Identify the parasite.
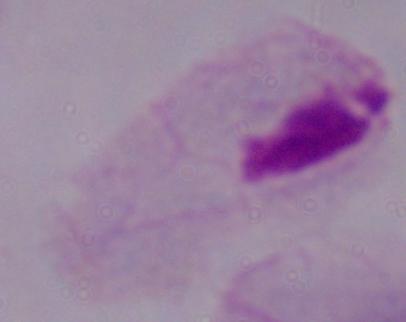

A trichomonad.

modality = micrograph
magnification = 1000x